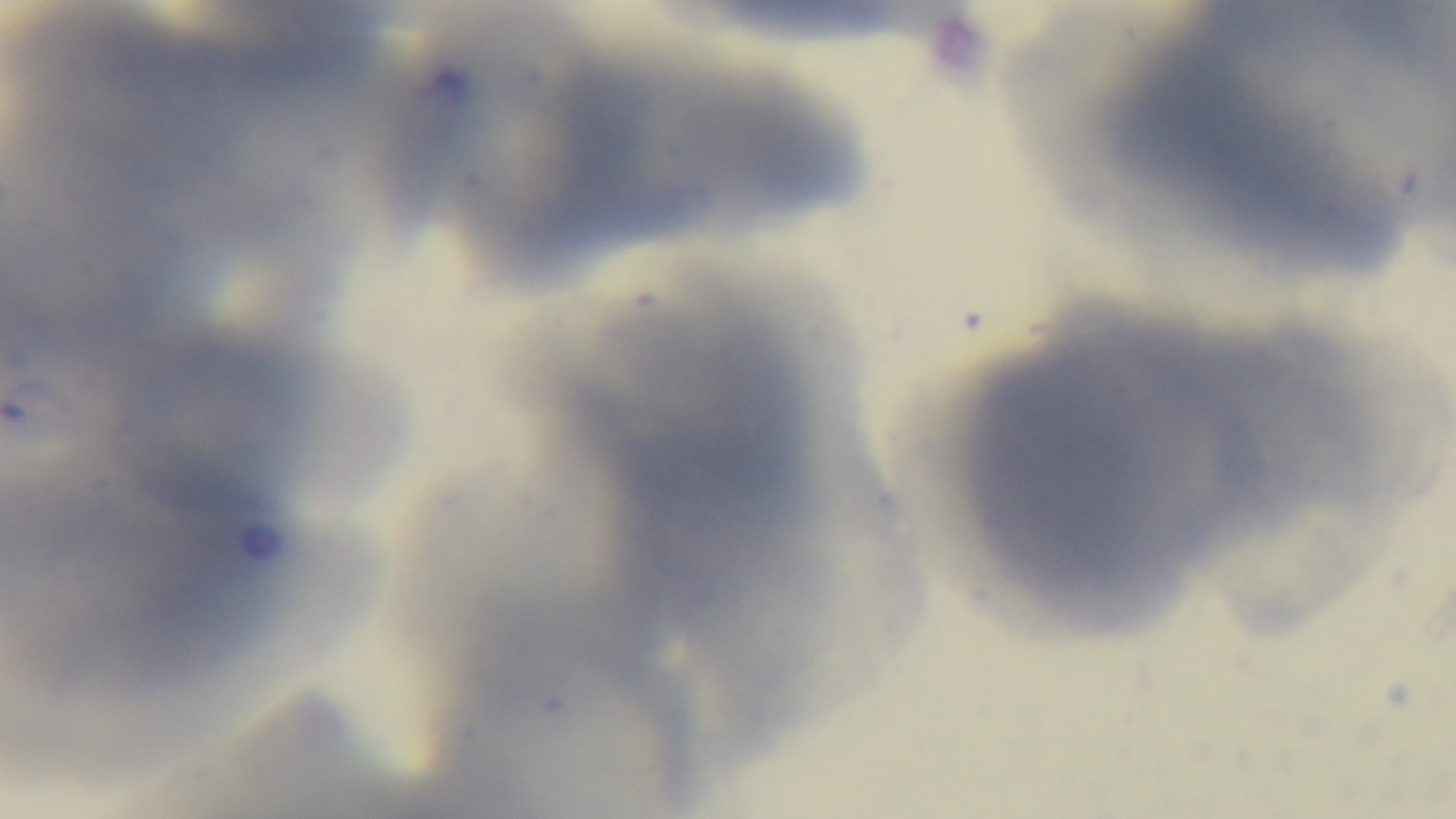

preparation = thin blood film
objective = 100x oil immersion
modality = light microscopy
capture = mounted 4K digital camera
field of view = one from the slide
stain = Giemsa
malaria status = uninfected